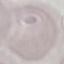
result = no malaria parasites detected
preparation = thin blood film
capture = smartphone camera at the microscope eyepiece
image type = cell patch, automatically extracted from a larger field of view and resized to 64 × 64 pixels
stain = Giemsa